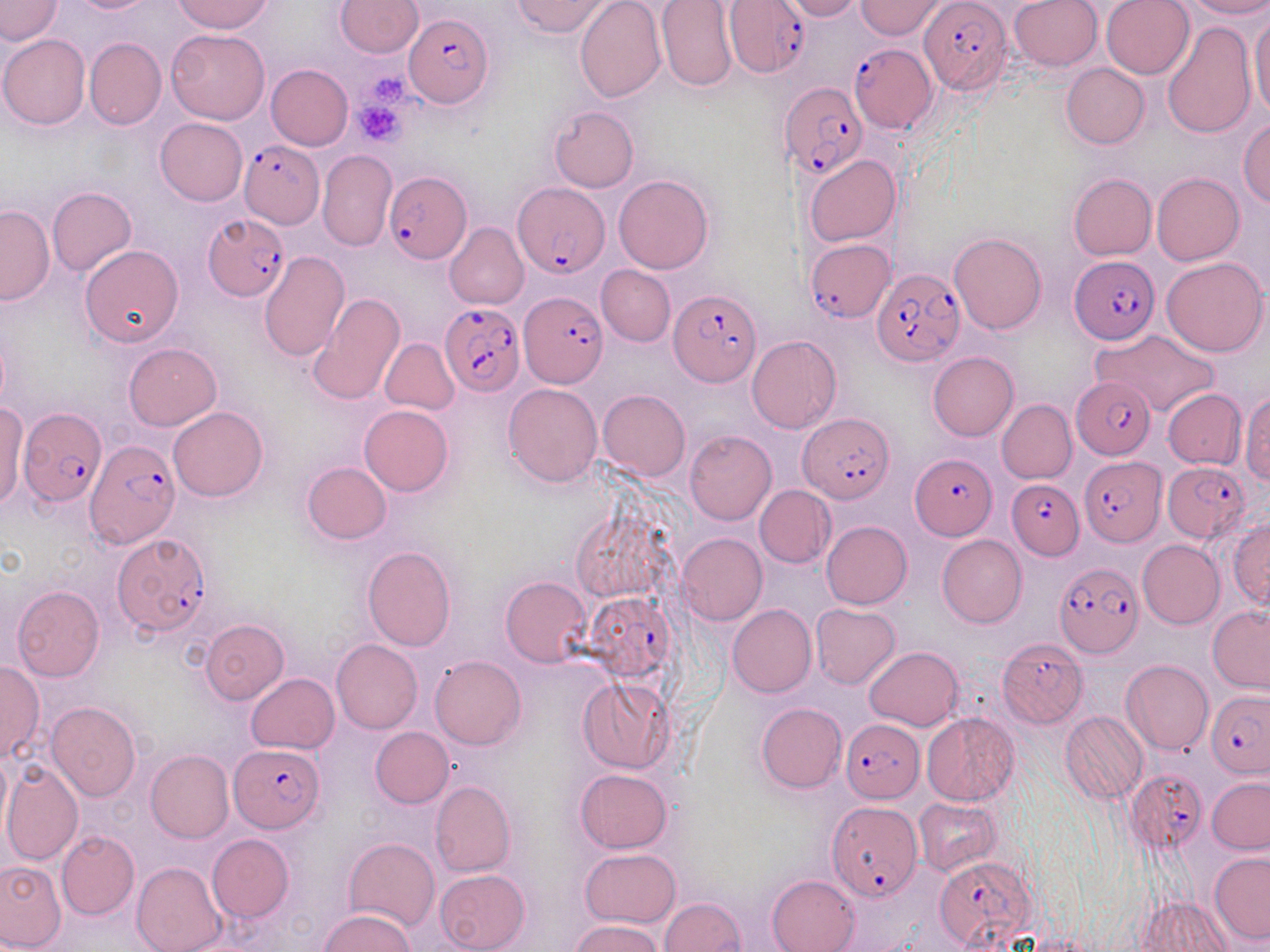
Plasmodium falciparum-infected red blood cell locations = approximate bounding boxes as (x1,y1)-(x2,y2) corner pairs in pixels: (725,1)-(811,78), (920,1)-(1010,94), (405,13)-(491,108), (851,42)-(939,133), (780,82)-(867,180), (237,138)-(323,227), (384,171)-(472,264), (514,182)-(607,278), (202,217)-(287,300), (805,238)-(894,320), (1070,256)-(1161,345), (871,267)-(967,367), (667,290)-(758,387), (520,292)-(607,388), (441,301)-(526,397), (1071,377)-(1157,459), (16,405)-(106,509), (799,413)-(894,502), (81,438)-(183,560), (911,452)-(997,539), (1081,454)-(1163,544), (1163,459)-(1250,541), (1007,479)-(1084,557), (112,533)-(211,637), (1054,563)-(1142,659), (585,593)-(675,680), (999,640)-(1088,726), (1206,689)-(1269,778), (842,719)-(924,802), (231,743)-(323,831), (1129,771)-(1204,855), (828,800)-(920,900), (934,855)-(1037,949)
slide-level diagnosis = Plasmodium falciparum
field of view = one of a larger specimen
image size = 1270×952 pixels
magnification = 1000x
preparation = thin blood film
uninfected red blood cell locations = approximate bounding boxes as (x1,y1)-(x2,y2) corner pairs in pixels: (0,0)-(63,45), (68,0)-(157,13), (174,0)-(273,34), (334,0)-(423,57), (511,0)-(613,37), (574,0)-(666,103), (1009,0)-(1103,71), (1102,0)-(1194,79), (1182,0)-(1270,19), (780,1)-(865,22), (855,1)-(948,39), (656,2)-(738,93), (1249,10)-(1270,121), (1163,22)-(1256,138), (166,28)-(270,124), (0,34)-(90,129), (85,37)-(166,130), (1061,63)-(1149,149), (265,64)-(353,150), (549,105)-(638,193), (155,118)-(248,206), (1239,119)-(1269,208), (318,149)-(396,250), (805,154)-(901,246), (1151,172)-(1243,265), (1068,173)-(1157,260), (613,174)-(714,274), (46,186)-(136,277), (0,204)-(53,306), (445,222)-(529,309), (949,233)-(1046,334), (80,244)-(185,346), (260,250)-(350,361), (1161,256)-(1267,357), (598,265)-(675,346), (307,293)-(406,407), (1093,329)-(1221,418), (747,335)-(843,434), (379,338)-(459,415), (123,342)-(221,430), (927,351)-(1018,440), (503,384)-(602,487), (1162,388)-(1246,470), (598,389)-(691,481), (1242,393)-(1270,483), (996,399)-(1077,483), (1,400)-(26,511), (359,404)-(455,496), (169,406)-(268,502), (684,430)-(776,525), (301,462)-(391,544), (755,485)-(836,568), (1229,516)-(1269,609), (822,521)-(912,609), (676,532)-(767,625), (937,535)-(1027,628), (1137,539)-(1224,629), (361,546)-(456,651), (500,576)-(591,667), (13,584)-(105,681), (810,603)-(900,689), (727,604)-(815,697), (1207,604)-(1270,693), (199,619)-(289,704), (332,640)-(423,734), (865,646)-(963,731), (430,654)-(526,750), (1121,659)-(1213,755), (0,660)-(44,764), (246,673)-(339,754), (577,675)-(675,774), (45,701)-(140,800), (756,702)-(846,792), (921,711)-(1020,805), (1061,712)-(1148,804), (370,726)-(454,808), (0,749)-(11,842), (146,749)-(234,844), (1,760)-(83,867), (574,769)-(671,854), (1207,777)-(1270,853), (431,780)-(515,878), (915,797)-(1001,876), (56,830)-(139,920), (207,834)-(294,922), (344,838)-(439,931), (580,848)-(680,928), (1209,851)-(1270,944), (0,861)-(66,950), (133,861)-(226,952), (435,868)-(530,952), (767,875)-(860,952), (1139,894)-(1234,952), (659,897)-(745,952), (318,909)-(417,952), (571,919)-(664,952)
modality = optical microscopy
platelet locations = approximate bounding boxes as (x1,y1)-(x2,y2) corner pairs in pixels: (371,73)-(410,106), (354,95)-(409,146)
stain = May-Grünwald-Giemsa